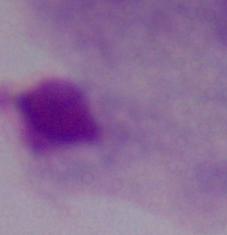
identification = trichomonad
modality = micrograph
magnification = 1000x